Report the malaria status of this cell.
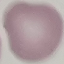

Uninfected.

Summary:
  - Image type: automatically extracted cell patch, resized to 64 × 64 pixels
  - Stain: Giemsa
  - Capture: smartphone camera at the microscope eyepiece
  - Preparation: thin blood film